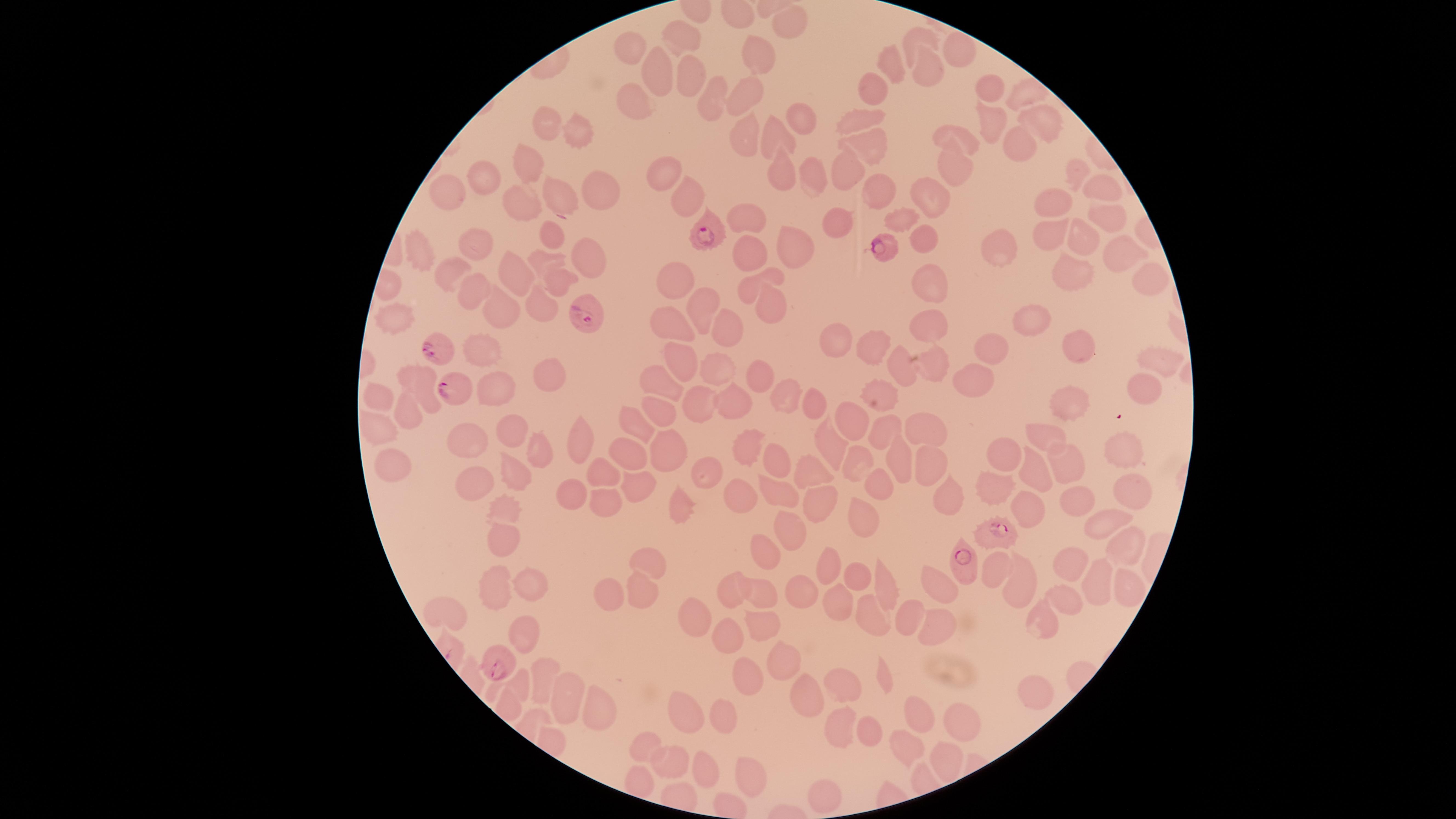
presence: malaria parasites identified
preparation: thin blood film
image_size: 1456×819 pixels
species: Plasmodium falciparum
field_of_view: single
capture: smartphone photograph through the microscope eyepiece
visible_region: circular
parasitized_RBCs: 'approximate marker points as (x, y) in pixels: (562, 198), (713, 235), (885, 250), (584, 314), (442, 352), (453, 386), (998, 534), (963, 565), (500, 666)'
stain: Giemsa
uninfected_RBCs: 'approximate marker points as (x, y) in pixels: (789, 18), (918, 40), (680, 42), (629, 48), (751, 53), (955, 54), (891, 61), (919, 69), (654, 70), (685, 76), (988, 87), (873, 89), (746, 91), (1023, 94), (713, 98), (631, 99), (859, 112), (800, 118), (983, 119), (1036, 119), (547, 122), (576, 130), (743, 137), (961, 138), (777, 139), (864, 145), (1013, 145), (952, 161), (526, 166), (780, 166), (846, 169), (1076, 169), (662, 172), (815, 173), (481, 179), (452, 189), (1101, 189), (596, 191), (1053, 197), (875, 198), (684, 201), (924, 204), (520, 205), (1099, 214), (749, 216), (902, 219), (833, 222), (551, 234), (1046, 235), (1078, 239), (921, 240), (998, 247), (477, 248), (747, 248), (788, 248), (1118, 252), (417, 256), (539, 260), (589, 260), (450, 270), (772, 272), (1069, 273), (516, 275), (678, 275), (1148, 277), (930, 280), (556, 282), (469, 300), (766, 303), (499, 304), (538, 305), (701, 307), (1032, 316), (390, 318), (673, 321), (925, 326), (729, 327), (838, 340), (1077, 341), (868, 345), (993, 346), (475, 354), (1150, 356), (933, 360), (678, 361), (900, 362), (712, 371), (754, 374), (547, 376), (418, 379), (976, 380), (655, 384), (1138, 387), (788, 393), (876, 393), (382, 397), (495, 398), (730, 401), (696, 402), (813, 402), (1068, 404), (653, 408), (406, 410), (858, 412), (639, 425), (887, 426), (924, 426), (379, 427), (1045, 434), (514, 435), (472, 439), (830, 441), (582, 442), (755, 442), (1007, 448), (1125, 448), (543, 451), (626, 451), (668, 454), (780, 457), (855, 461), (389, 462), (901, 463), (1035, 463), (1067, 466), (925, 467), (815, 472), (512, 473), (601, 473), (705, 476), (881, 484), (988, 484), (472, 485), (638, 488), (571, 489), (1128, 493), (732, 497), (778, 497), (949, 497), (1072, 497), (673, 501), (818, 501), (599, 502), (1028, 506), (499, 510), (862, 515), (1104, 525), (784, 534), (501, 535), (759, 553), (1125, 553), (1068, 560), (649, 562), (1003, 565), (828, 568), (858, 580), (1097, 580), (530, 583), (1025, 584), (497, 585), (888, 588), (802, 589), (938, 589), (1127, 589), (729, 592), (639, 594), (760, 596), (1061, 597), (605, 598), (834, 601), (448, 611), (699, 617), (870, 618), (933, 619), (910, 621), (1038, 621), (759, 624), (522, 630), (726, 639), (785, 664), (738, 674), (521, 680), (543, 680), (838, 684), (1030, 692), (567, 697), (809, 699), (601, 710), (919, 710), (684, 714), (720, 718), (961, 721), (842, 730), (871, 736), (648, 748), (903, 748), (670, 756), (946, 759), (710, 768), (751, 776), (819, 791)'